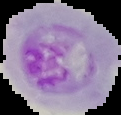
image type = cell region segmented out of the field of view; surrounding area masked to black
image size = 121×115 pixels
preparation = thin blood film
result = malaria parasites detected